Name the blood parasite species.
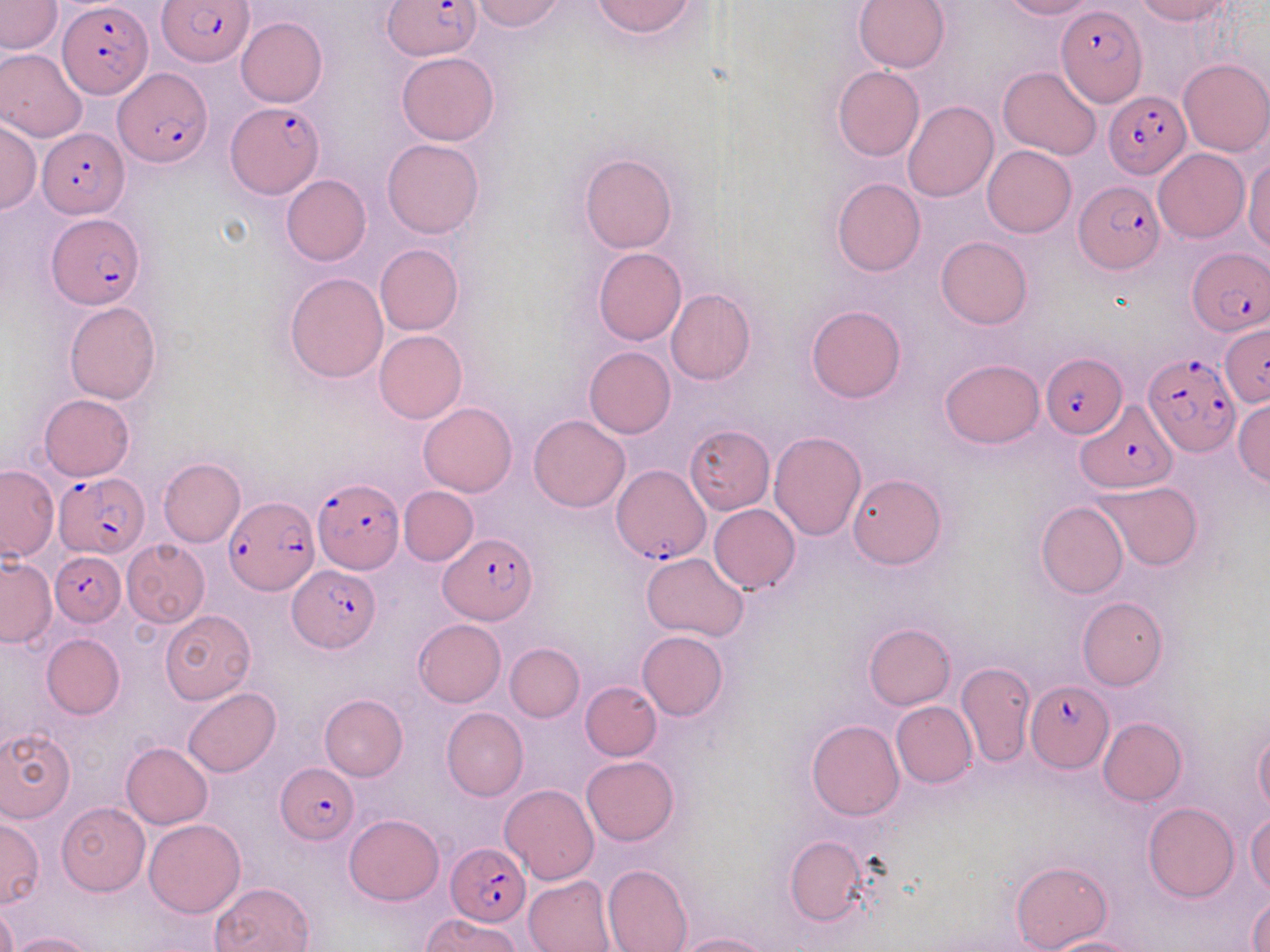

Plasmodium falciparum.

stain = May-Grünwald-Giemsa
modality = light microscopy
Plasmodium falciparum-infected red blood cell locations = approximate bounding boxes as [x1, y1, x2, y2] in pixels: [158, 0, 254, 68], [382, 0, 479, 60], [59, 1, 152, 101], [1057, 6, 1147, 105], [114, 66, 211, 166], [1103, 90, 1190, 177], [226, 101, 323, 197], [38, 127, 127, 216], [1073, 179, 1163, 275], [45, 214, 147, 310], [1187, 248, 1269, 336], [1220, 325, 1270, 406], [1042, 352, 1126, 442], [1143, 352, 1239, 456], [1075, 401, 1179, 496], [611, 465, 709, 563], [55, 473, 149, 557], [312, 478, 403, 573], [225, 497, 317, 595], [440, 532, 535, 623], [49, 550, 125, 627], [288, 565, 380, 653], [1026, 680, 1114, 771], [275, 763, 358, 843], [447, 842, 529, 924]
field of view = one of a larger specimen
preparation = thin blood smear
image size = 1270×952 pixels
uninfected red blood cell locations = approximate bounding boxes as [x1, y1, x2, y2] in pixels: [470, 0, 567, 32], [591, 0, 698, 37], [851, 0, 950, 72], [998, 0, 1098, 20], [1132, 0, 1231, 24], [0, 1, 62, 53], [236, 17, 327, 106], [0, 48, 88, 142], [396, 51, 500, 147], [1179, 58, 1270, 156], [832, 66, 924, 161], [998, 66, 1102, 160], [902, 101, 997, 202], [0, 120, 41, 213], [382, 138, 483, 238], [982, 145, 1076, 238], [1153, 148, 1249, 243], [580, 153, 678, 253], [1244, 155, 1270, 253], [281, 174, 370, 266], [832, 178, 925, 277], [936, 236, 1032, 328], [375, 243, 462, 336], [593, 248, 686, 345], [284, 272, 389, 382], [666, 289, 756, 385], [64, 300, 162, 404], [806, 304, 906, 403], [374, 330, 467, 424], [584, 346, 677, 439], [939, 358, 1046, 449], [39, 394, 134, 480], [1232, 398, 1270, 488], [419, 402, 517, 497], [529, 415, 630, 512], [684, 425, 775, 514], [769, 431, 865, 540], [158, 458, 245, 547], [0, 466, 58, 563], [846, 473, 947, 569], [1090, 479, 1203, 571], [399, 486, 478, 565], [1036, 502, 1128, 598], [709, 504, 801, 594], [122, 540, 210, 627], [640, 551, 748, 643], [0, 556, 55, 647], [1078, 597, 1167, 689], [160, 610, 257, 704], [413, 619, 506, 707], [863, 622, 955, 708], [636, 630, 729, 720], [42, 634, 125, 718], [505, 643, 584, 721], [956, 661, 1036, 768], [581, 681, 661, 760], [184, 688, 280, 777], [319, 694, 408, 781], [891, 701, 976, 788], [442, 708, 529, 801], [1098, 716, 1186, 804], [806, 720, 903, 821], [0, 728, 75, 821], [1254, 729, 1270, 818], [121, 743, 212, 829], [582, 755, 679, 845], [500, 784, 598, 884], [57, 801, 149, 895], [1143, 803, 1238, 902], [1247, 810, 1270, 895], [344, 814, 444, 905], [145, 819, 245, 918], [0, 820, 43, 907], [784, 835, 871, 928], [1012, 860, 1112, 951], [603, 863, 693, 952], [522, 874, 614, 952], [210, 881, 316, 952], [1248, 893, 1270, 950], [0, 904, 19, 952], [421, 913, 523, 952], [7, 932, 98, 952], [672, 932, 775, 952], [1042, 936, 1140, 952]
magnification = 1000x